Describe the morphology of the red blood cells.
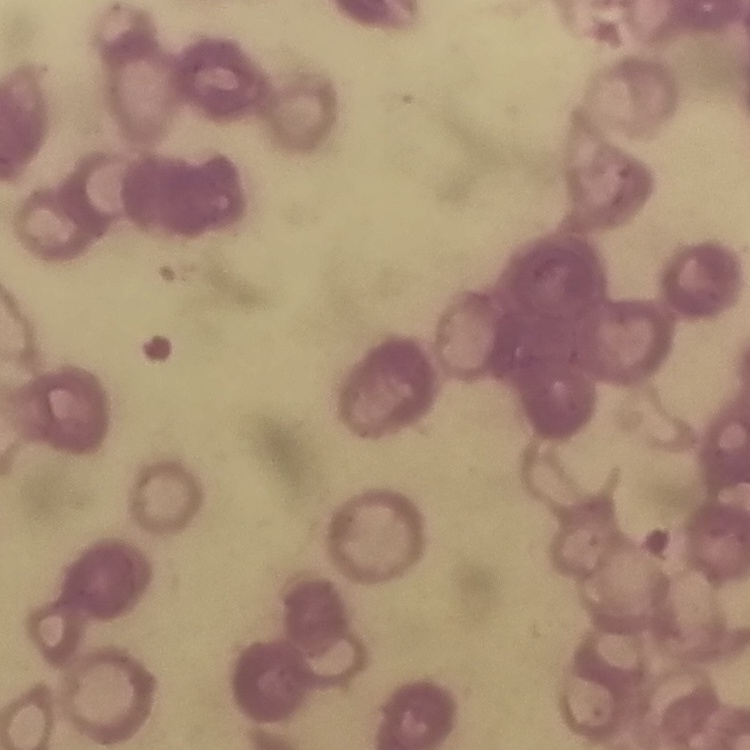
Rouleaux formation.

Stained with either Field's or Giemsa. One tile cut from a larger photomicrograph. Thin blood film.